Report the malaria status.
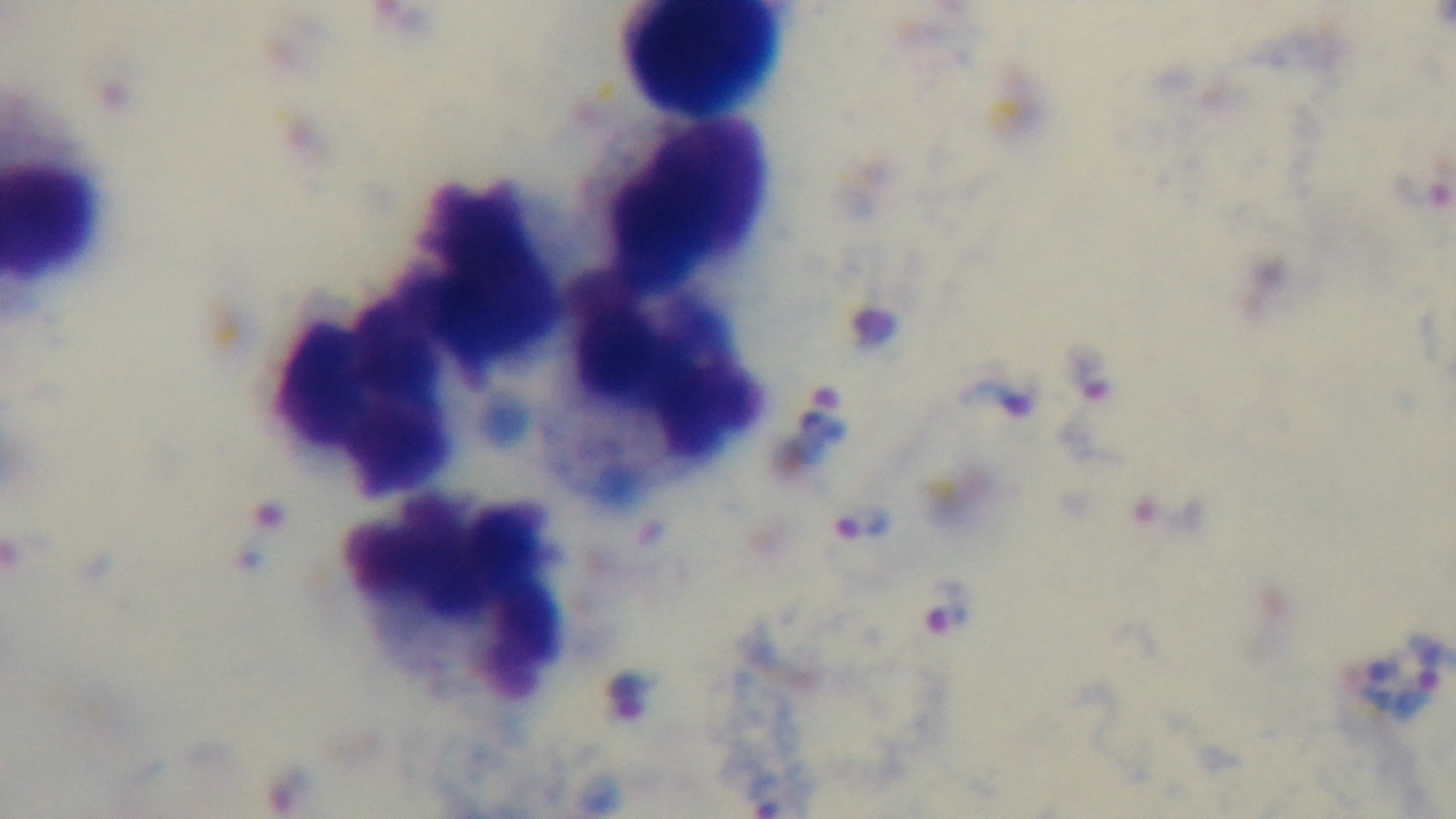
Positive.

Mounted 4K digital camera. Giemsa stain. 100x oil-immersion objective. Photomicrograph. One field from the slide. Preparation: thick smear.